Report the malaria status of this cell.
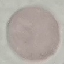

Uninfected.

stain = Giemsa
preparation = thin smear
capture = smartphone through the microscope eyepiece
image type = cell patch, automatically extracted from a larger field of view and resized to 64 × 64 pixels